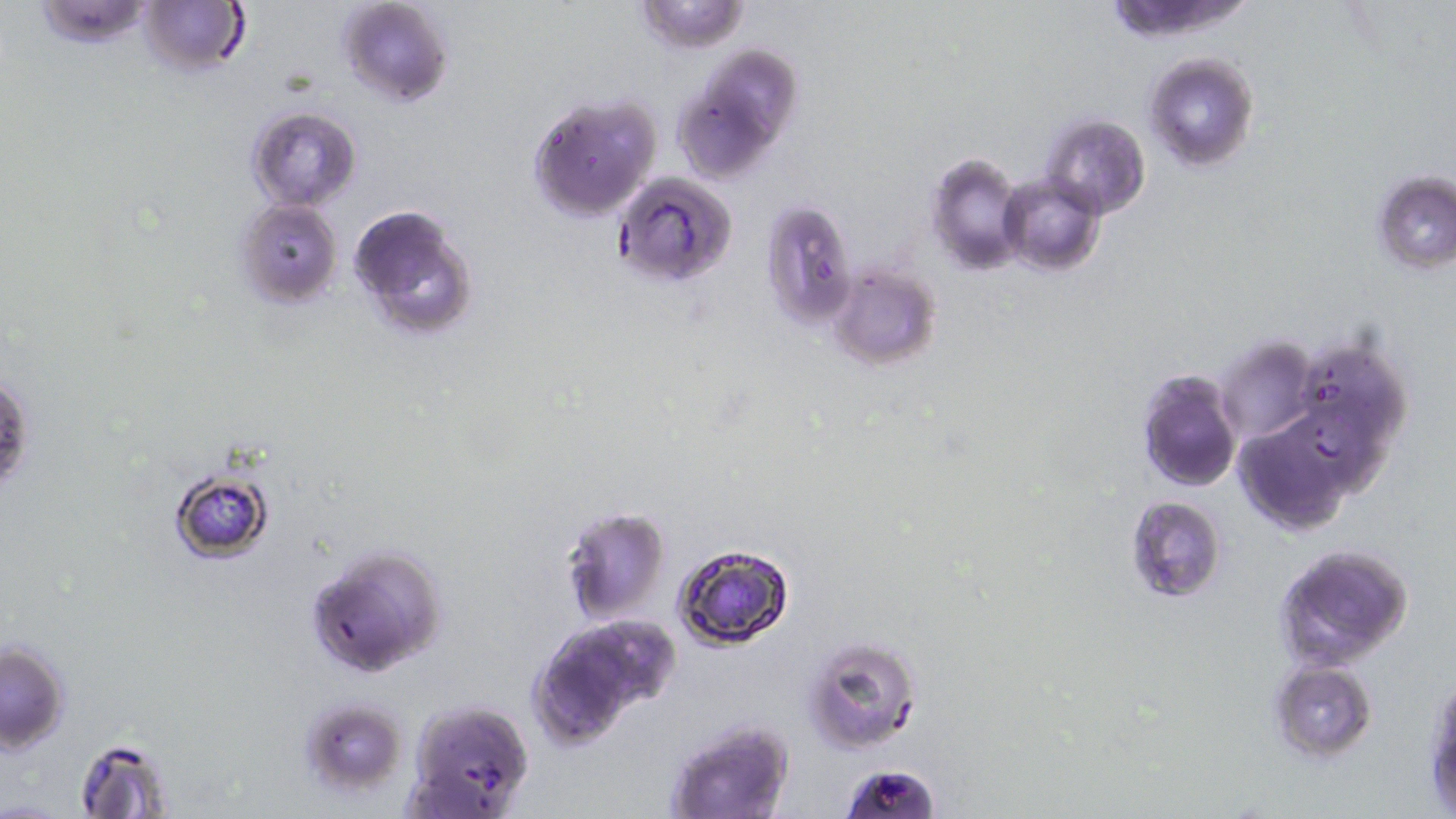

Summary:
  - Coordinate format: approximate bounding boxes as (x1,y1)-(x2,y2) corner pairs in pixels
  - Uninfected red blood cell locations: (30,0)-(159,48), (336,0)-(454,107), (633,0)-(751,53), (138,1)-(247,77), (704,45)-(802,141), (1144,52)-(1259,173), (677,93)-(768,186), (527,94)-(662,221), (247,107)-(360,208), (1042,114)-(1149,219), (925,152)-(1026,275), (1370,171)-(1455,274), (613,172)-(738,288), (998,176)-(1104,275), (236,198)-(341,307), (760,198)-(860,328), (347,203)-(479,342), (826,262)-(943,369), (1217,337)-(1317,443), (1306,349)-(1409,426), (1135,369)-(1243,494), (1280,406)-(1400,489), (1235,424)-(1349,532), (167,467)-(277,564), (1125,495)-(1226,602), (558,504)-(670,624), (671,541)-(795,651), (305,543)-(447,678), (1272,543)-(1414,671), (530,619)-(670,746), (803,636)-(922,754), (0,640)-(71,753), (1267,660)-(1376,762), (1425,675)-(1455,809), (297,695)-(406,798), (402,699)-(534,817), (660,715)-(796,819), (75,736)-(177,818), (841,762)-(938,819)
  - Slide-level diagnosis: Plasmodium falciparum
  - Modality: light microscopy
  - Stain: May-Grünwald-Giemsa
  - Image size: 1456×819 pixels
  - Field of view: one of a larger specimen
  - Preparation: thin blood film
  - Magnification: 1000x